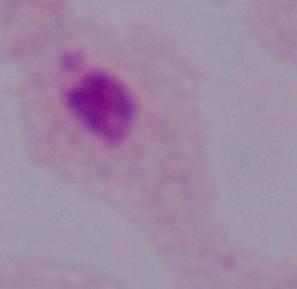
Summary:
  - Magnification: 1000x
  - Modality: photomicrograph
  - Identification: trichomonad